Report the malaria status of this cell.
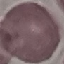
It is uninfected.

stain = Giemsa
capture = smartphone camera at the microscope eyepiece
image type = automatically extracted cell patch, resized to 64 × 64 pixels
preparation = thin blood film